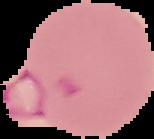

Summary:
  - Result: malaria parasites detected
  - Preparation: thin blood smear
  - Image size: 154×139 pixels
  - Image type: segmented cell region on a black background